Outline platelets.
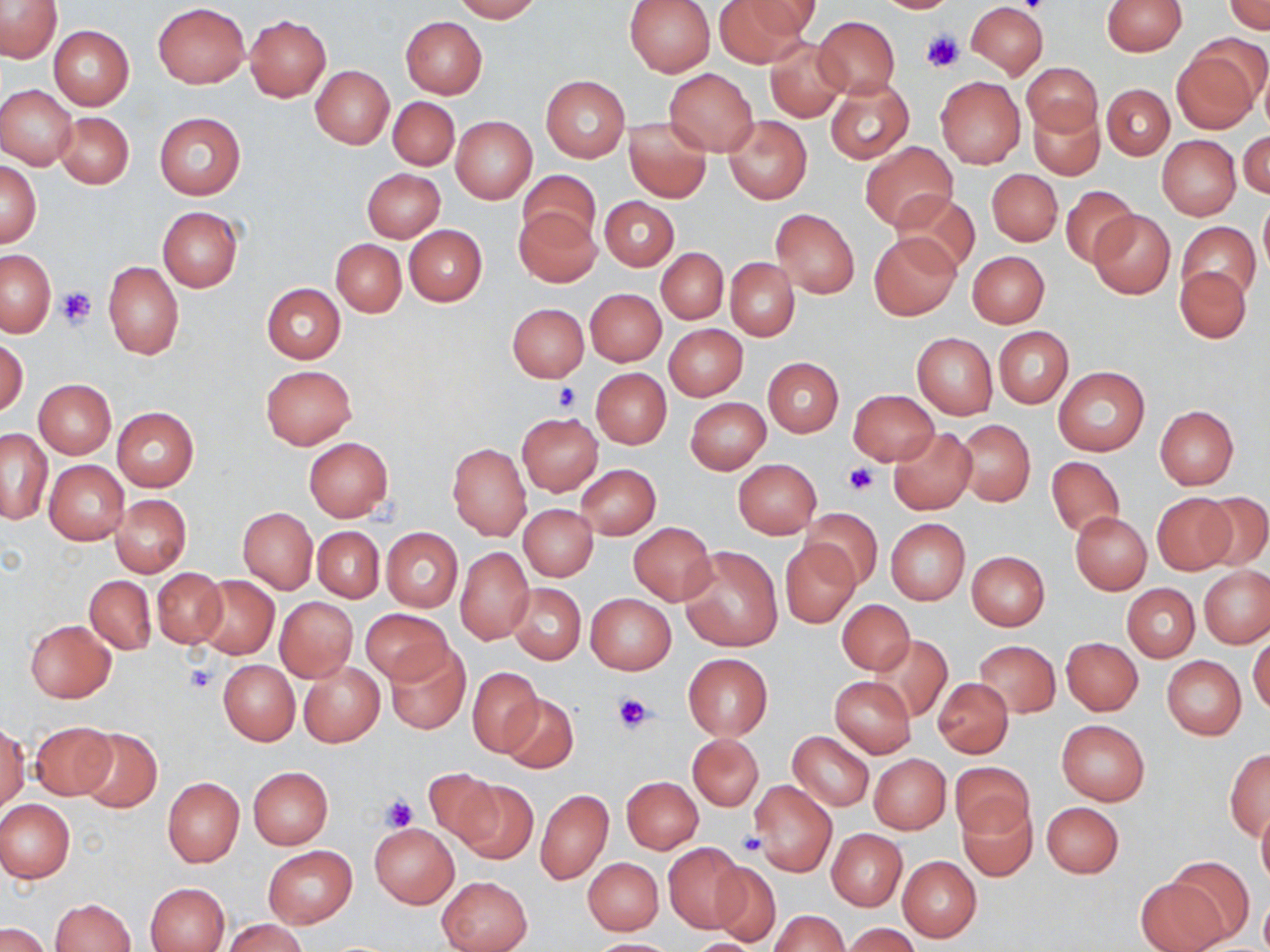

Approximate bounding boxes as [x1, y1, x2, y2] in pixels.
Platelets: [922, 31, 964, 74], [56, 288, 95, 328], [554, 383, 581, 411], [844, 462, 878, 496], [185, 664, 217, 695], [612, 691, 655, 733], [378, 793, 417, 832], [736, 832, 765, 856].

Uninfected red blood cell locations: [0, 0, 64, 63], [452, 0, 542, 22], [624, 0, 715, 76], [715, 0, 813, 65], [743, 0, 824, 39], [872, 0, 957, 13], [1101, 0, 1187, 55], [965, 2, 1048, 79], [1225, 2, 1270, 35], [153, 3, 250, 88], [244, 15, 331, 102], [813, 16, 900, 99], [400, 17, 487, 97], [49, 27, 134, 109], [765, 38, 849, 122], [1171, 46, 1261, 135], [1023, 62, 1101, 137], [312, 66, 393, 148], [665, 68, 758, 155], [540, 76, 629, 162], [935, 76, 1025, 168], [825, 77, 913, 165], [1102, 84, 1174, 159], [0, 85, 77, 168], [388, 97, 459, 169], [1029, 104, 1103, 180], [54, 112, 134, 188], [154, 112, 245, 199], [723, 115, 811, 204], [451, 116, 537, 202], [623, 116, 711, 203], [1239, 130, 1269, 199], [1156, 136, 1240, 221], [861, 142, 957, 231], [0, 158, 40, 248], [363, 168, 445, 242], [987, 168, 1062, 246], [518, 170, 599, 246], [1059, 185, 1139, 269], [891, 190, 979, 278], [600, 196, 678, 270], [1258, 201, 1270, 278], [514, 206, 599, 286], [157, 207, 242, 292], [771, 209, 859, 297], [1090, 211, 1174, 298], [1179, 220, 1260, 305], [404, 224, 487, 306], [869, 233, 960, 319], [331, 239, 407, 317], [657, 248, 728, 323], [1, 250, 55, 335], [967, 251, 1049, 327], [726, 257, 799, 340], [104, 261, 183, 360], [1175, 266, 1252, 343], [261, 283, 345, 363], [585, 288, 666, 366], [507, 303, 588, 381], [664, 324, 747, 401], [993, 326, 1073, 408], [912, 333, 997, 419], [1, 337, 28, 417], [763, 357, 843, 438], [260, 364, 357, 450], [1054, 366, 1149, 455], [591, 368, 670, 448], [34, 378, 116, 458], [847, 390, 938, 467], [685, 397, 770, 474], [1154, 406, 1238, 488], [112, 407, 199, 490], [516, 412, 603, 494], [956, 419, 1035, 507], [888, 428, 976, 514], [1, 429, 51, 525], [304, 436, 394, 522], [447, 442, 531, 540], [1046, 456, 1123, 541], [733, 458, 822, 539], [44, 460, 129, 545], [576, 465, 660, 539], [1199, 492, 1270, 573], [1152, 493, 1239, 575], [110, 494, 191, 577], [519, 504, 598, 580], [238, 507, 317, 593], [802, 508, 883, 588], [1070, 512, 1152, 594], [885, 518, 969, 605], [628, 522, 716, 605], [313, 527, 384, 601], [381, 528, 463, 612], [780, 541, 860, 628], [679, 546, 782, 652], [456, 547, 535, 644], [966, 551, 1049, 631], [1200, 567, 1269, 648], [152, 568, 227, 648], [195, 575, 279, 659], [85, 576, 155, 654], [507, 582, 586, 665], [1123, 584, 1200, 662], [586, 593, 676, 674], [275, 596, 357, 682], [838, 599, 914, 673], [360, 608, 453, 685], [24, 619, 116, 703], [1249, 632, 1270, 717], [870, 635, 952, 723], [1061, 637, 1143, 716], [975, 641, 1060, 717], [386, 642, 470, 736], [682, 653, 772, 739], [1161, 655, 1246, 740], [218, 659, 299, 745], [298, 661, 384, 746], [468, 666, 542, 756], [830, 676, 915, 757], [934, 678, 1013, 757], [500, 694, 578, 772], [1056, 719, 1150, 806], [29, 721, 117, 801], [0, 723, 28, 811], [76, 727, 162, 813], [788, 731, 874, 811], [688, 734, 763, 810], [1224, 749, 1270, 840], [870, 754, 951, 833], [951, 762, 1032, 839], [248, 766, 333, 849], [425, 770, 503, 848], [622, 776, 702, 853], [162, 777, 244, 867], [455, 779, 538, 864], [750, 780, 836, 877], [536, 788, 613, 884], [0, 799, 75, 883], [958, 800, 1037, 882], [1042, 801, 1123, 878], [1258, 806, 1270, 890], [370, 823, 460, 909], [827, 829, 907, 911], [663, 843, 745, 932], [263, 846, 357, 928], [898, 856, 981, 942], [582, 857, 663, 934], [1165, 857, 1255, 943], [707, 862, 784, 946], [437, 875, 532, 952], [1136, 877, 1226, 952], [145, 882, 230, 951], [1259, 894, 1270, 952], [50, 898, 135, 952], [770, 910, 848, 952], [222, 918, 308, 952], [2, 923, 51, 952], [842, 923, 919, 952], [588, 938, 677, 951], [686, 938, 764, 951]. Slide-level diagnosis: no evidence of blood parasites. May-Grünwald-Giemsa stain. Single field of view. Thin blood film. Captured at 1000x magnification. Image is 1270×952 pixels. Optical microscopy.